Report the malaria status of this cell.
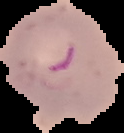
It is parasitized.

Summary:
  - Preparation: thin blood smear
  - Image type: segmented cell region with the area outside set to black
  - Image size: 124×133 pixels